Name the cell type shown.
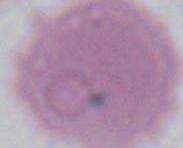

An erythrocyte.

Summary:
  - Magnification: 1000x
  - Modality: micrograph